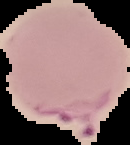 Image is 130×145 pixels. From a thin blood smear. Malaria status: parasitized. The area outside the segmented cell region is set to black.